Outline each Plasmodium falciparum-infected red blood cell.
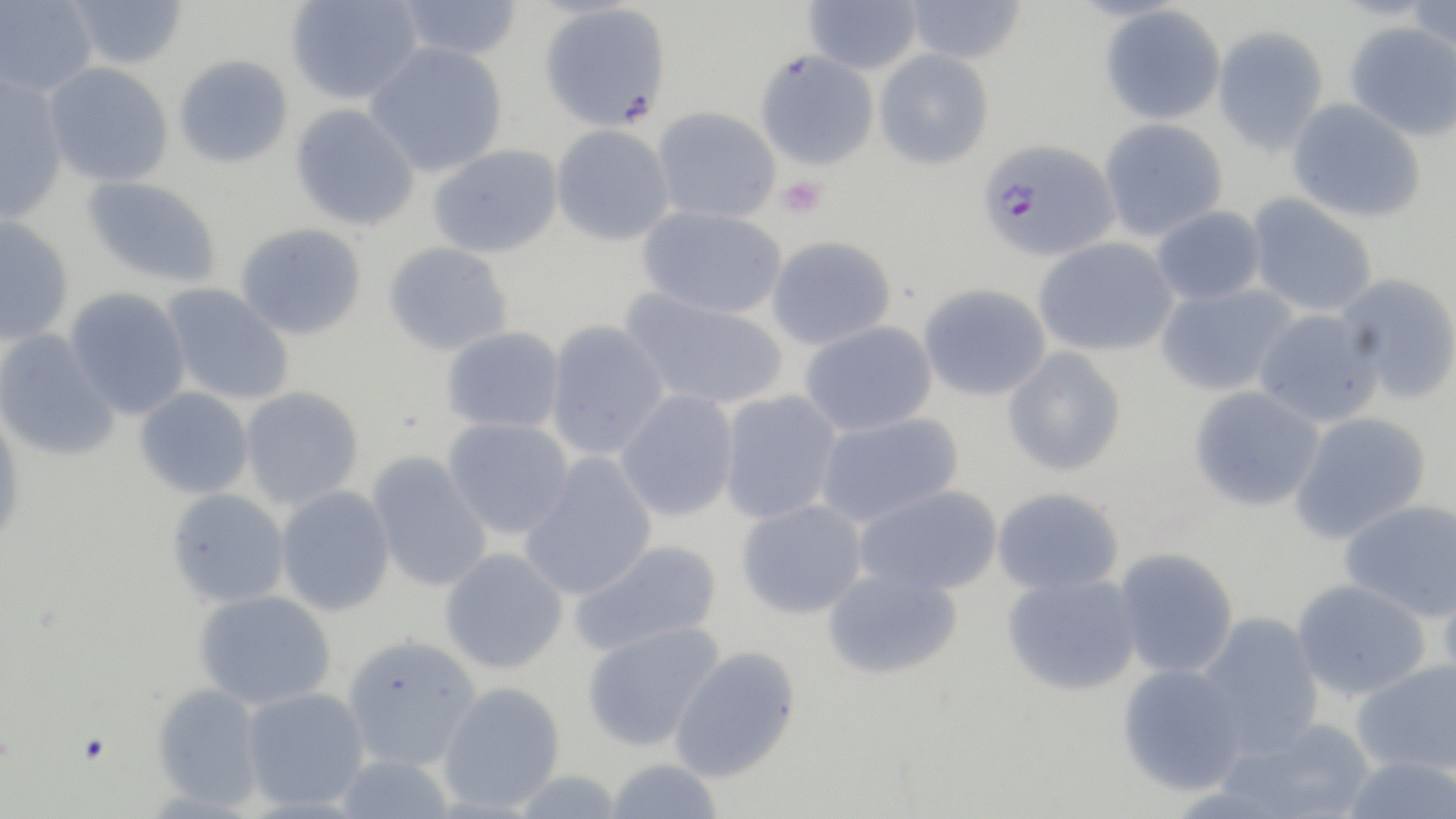
Approximate bounding boxes as (x1,y1)-(x2,y2) corner pairs in pixels.
Plasmodium falciparum-infected red blood cells: (976,139)-(1120,261).

Summary:
  - Uninfected red blood cell locations: (66,0)-(187,70), (286,0)-(422,105), (395,0)-(523,61), (802,0)-(922,74), (903,0)-(1026,64), (0,1)-(99,97), (1406,2)-(1456,59), (538,4)-(672,132), (1099,4)-(1226,126), (1344,21)-(1456,141), (1212,25)-(1329,157), (365,42)-(508,177), (873,49)-(994,170), (754,50)-(879,170), (173,54)-(293,168), (43,62)-(174,187), (0,73)-(69,223), (1286,98)-(1427,224), (290,103)-(421,231), (652,107)-(781,224), (1099,118)-(1228,241), (550,124)-(675,246), (428,144)-(564,259), (81,176)-(222,288), (1246,193)-(1378,318), (637,205)-(787,320), (1151,205)-(1266,306), (0,214)-(74,346), (236,223)-(367,340), (766,236)-(896,351), (1033,237)-(1179,357), (383,241)-(513,356), (1335,273)-(1456,404), (160,282)-(294,405), (1154,282)-(1298,397), (917,283)-(1051,401), (65,287)-(192,420), (621,289)-(789,411), (1252,307)-(1385,428), (544,319)-(670,460), (800,320)-(938,437), (441,326)-(565,433), (0,329)-(121,462), (1002,347)-(1127,477), (1188,385)-(1325,512), (134,386)-(254,499), (240,386)-(364,510), (614,389)-(739,522), (717,390)-(842,524), (0,409)-(26,548), (814,411)-(965,526), (1288,411)-(1432,544), (443,417)-(574,539), (367,452)-(492,592), (519,452)-(658,601), (854,484)-(1004,597), (275,486)-(395,616), (991,487)-(1125,596), (165,488)-(290,607), (735,498)-(868,620), (1339,498)-(1456,622), (569,538)-(723,656), (439,547)-(569,674), (1113,548)-(1239,678), (823,567)-(963,680), (1001,572)-(1141,696), (1438,576)-(1456,694), (1290,578)-(1432,700), (193,590)-(336,709), (1196,611)-(1325,755), (582,620)-(725,752), (342,635)-(482,770), (669,646)-(801,783), (1351,659)-(1456,776), (1116,663)-(1249,796), (438,681)-(566,813), (151,682)-(266,809), (241,686)-(370,812), (1221,715)-(1376,819), (332,752)-(457,819), (1339,754)-(1456,818), (604,758)-(723,819)
  - Platelet locations: (776,176)-(827,219)
  - Slide-level diagnosis: Plasmodium falciparum
  - Modality: light microscopy
  - Image size: 1456×819 pixels
  - Field of view: single
  - Stain: May-Grünwald-Giemsa
  - Preparation: thin blood film
  - Magnification: 1000x